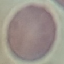
result = no malaria parasites detected
stain = Giemsa
image type = cell patch, automatically extracted from a larger field of view and resized to 64 × 64 pixels
preparation = thin blood smear
capture = smartphone camera at the microscope eyepiece